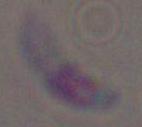
{
  "identification": "Toxoplasma gondii",
  "magnification": "1000x",
  "modality": "photomicrograph"
}